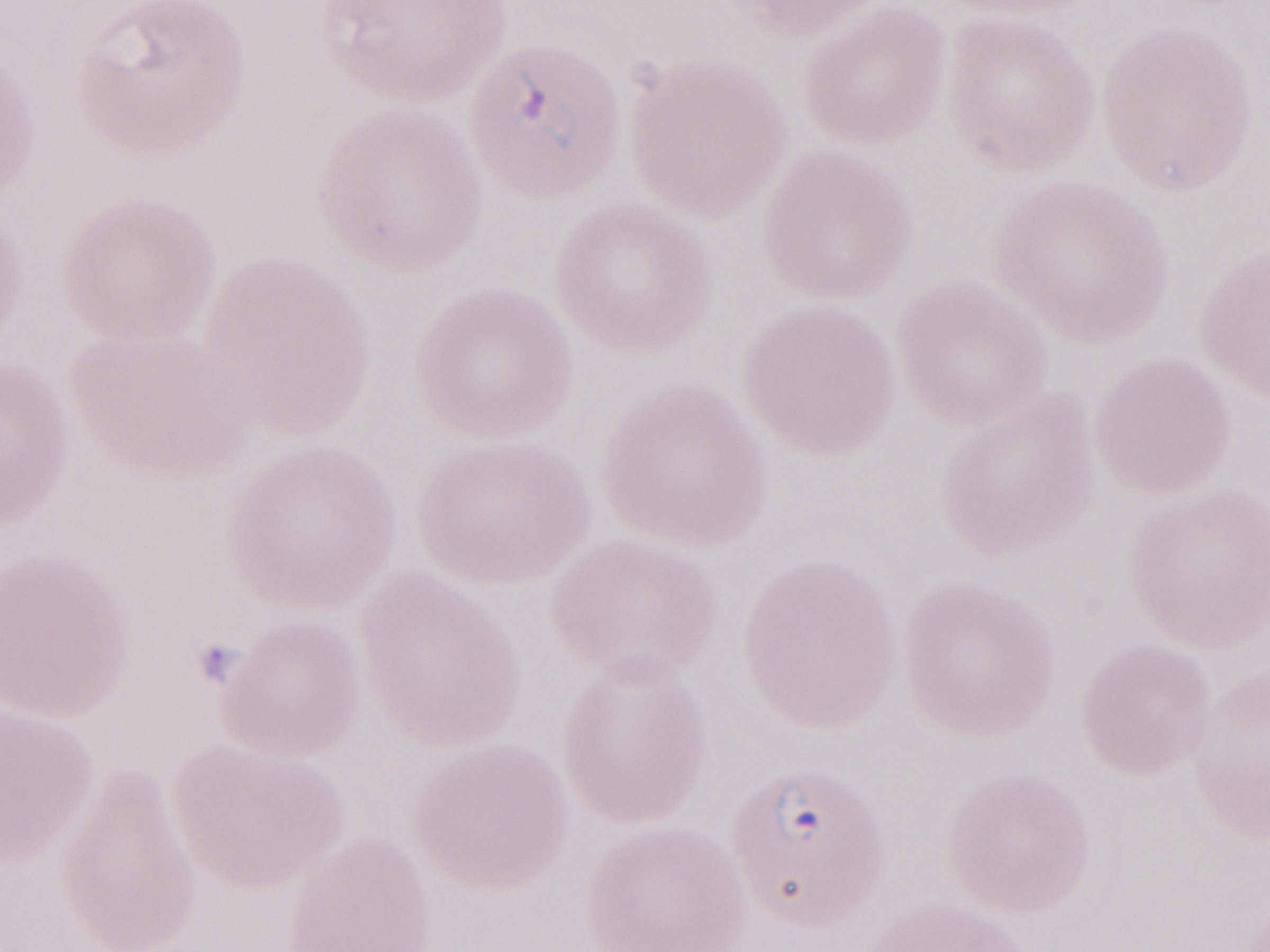

Patient diagnosis: malaria infection. Image is 1270×952 pixels. Thin peripheral-blood smear. May-Grünwald-Giemsa (MGG) stain. Olympus BX43 microscope, Olympus DP73 camera. 1,000x magnification. One field of this slide.